Give the position of every leukocyte visible.
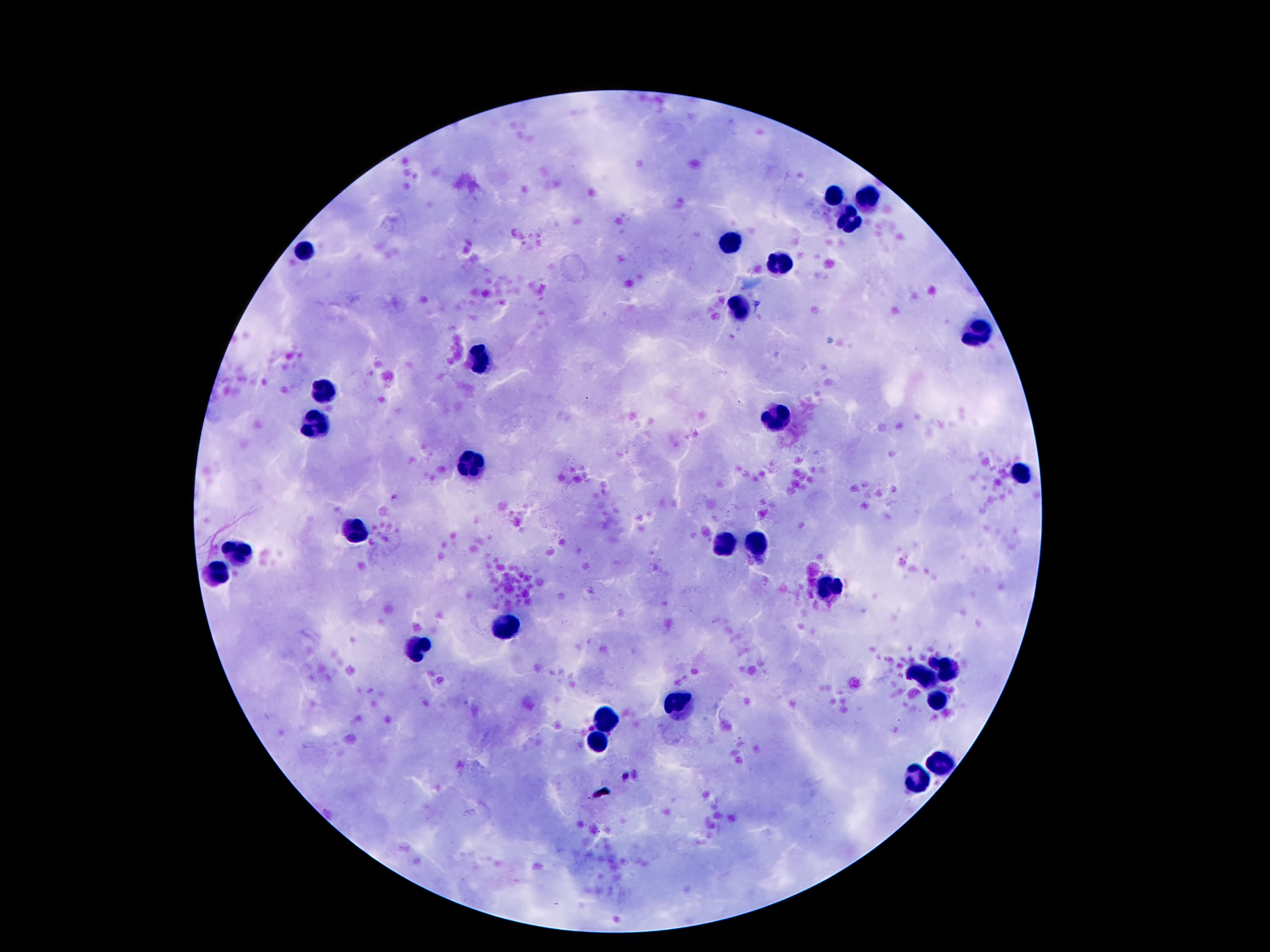

Approximate centers as (x, y) in pixels.
Leukocytes: (834, 197), (867, 197), (850, 220), (731, 243), (304, 245), (778, 262), (740, 309), (983, 337), (477, 361), (324, 389), (774, 421), (313, 428), (475, 464), (1022, 473), (354, 531), (755, 544), (722, 545), (242, 546), (212, 570), (826, 589), (509, 628), (417, 645), (949, 670), (927, 675), (936, 699), (679, 703), (606, 721), (595, 741), (938, 762), (921, 780).

capture = smartphone camera through the microscope eyepiece
patient malaria status = not infected
stain = Giemsa
preparation = thick blood film
image size = 1270×952 pixels
magnification = 100x
field of view = single